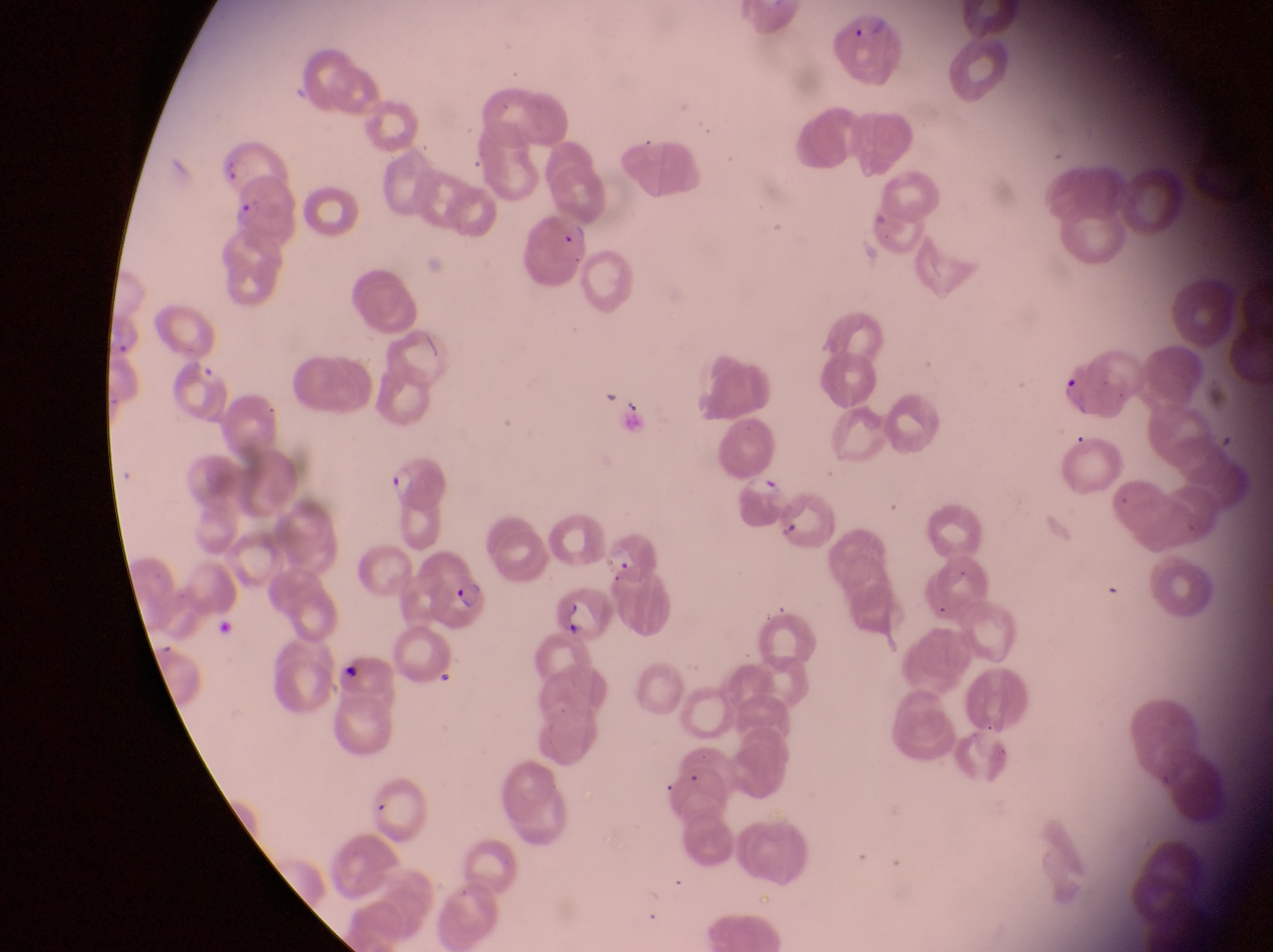
Approximate bounding boxes as [left, top, right, bottom] in pixels.
Summary:
  - Parasitised red blood cell locations: [837, 18, 906, 79], [240, 175, 302, 240], [519, 212, 595, 285], [174, 355, 232, 420], [1057, 359, 1131, 420], [391, 450, 453, 515], [743, 475, 795, 535], [604, 534, 662, 587], [434, 570, 492, 637], [554, 587, 616, 650]
  - Country: Uganda
  - Magnification: 1000x
  - Field of view: single
  - Preparation: thin blood film
  - Image size: 1273×952 pixels
  - Capture: smartphone photograph through the eyepiece of an Olympus CX-23 microscope